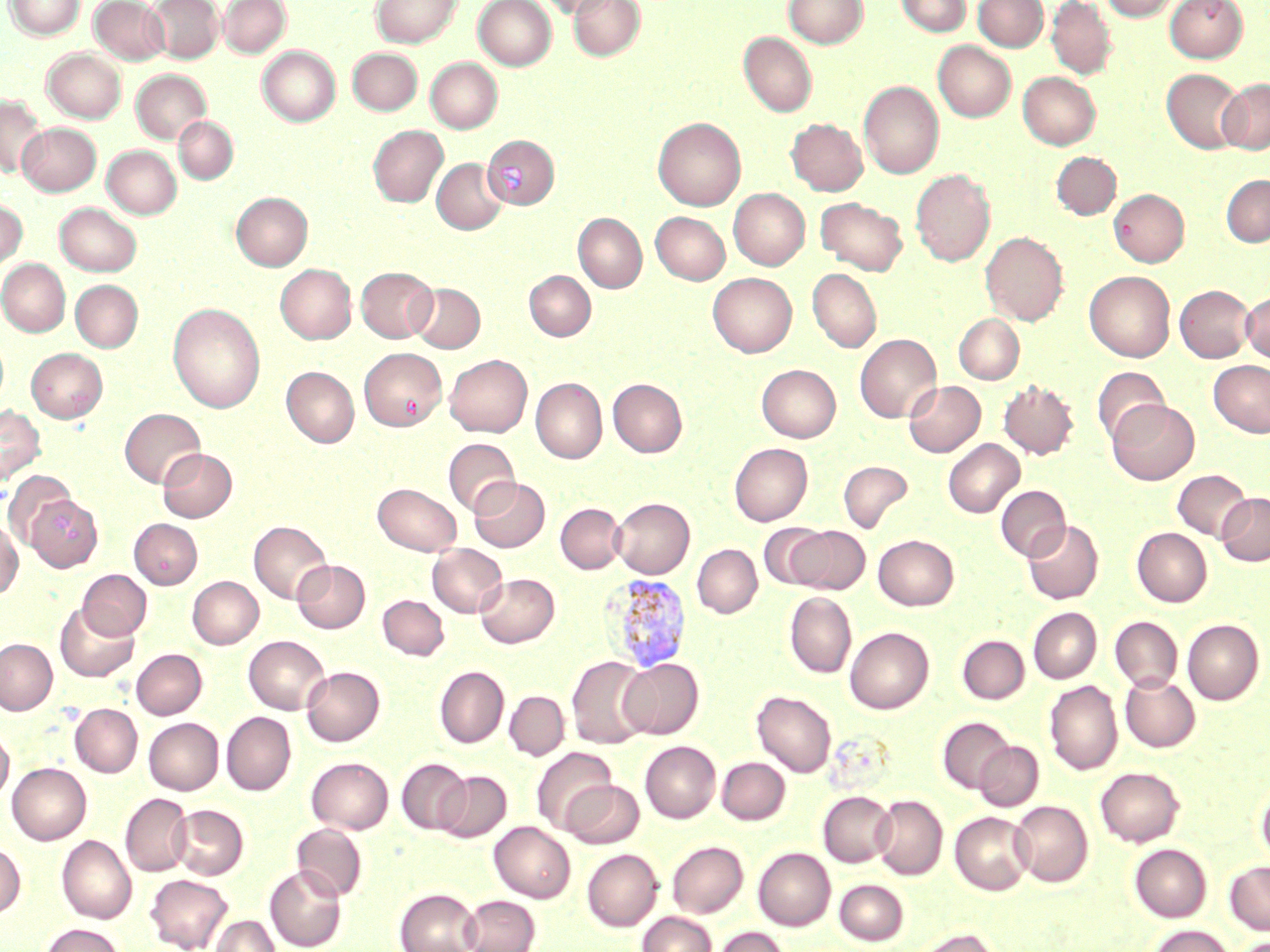

slide-level diagnosis = Plasmodium vivax
uninfected red blood cell locations = approximate bounding boxes as named x1/y1/x2/y2 corners in pixels: (x1=4, y1=0, x2=85, y2=40), (x1=90, y1=0, x2=169, y2=65), (x1=146, y1=0, x2=223, y2=63), (x1=219, y1=0, x2=291, y2=57), (x1=371, y1=0, x2=462, y2=47), (x1=474, y1=0, x2=556, y2=70), (x1=539, y1=0, x2=616, y2=18), (x1=569, y1=0, x2=644, y2=61), (x1=784, y1=0, x2=867, y2=49), (x1=896, y1=0, x2=971, y2=36), (x1=973, y1=0, x2=1048, y2=51), (x1=1046, y1=0, x2=1116, y2=79), (x1=1099, y1=0, x2=1182, y2=21), (x1=1165, y1=0, x2=1248, y2=62), (x1=739, y1=32, x2=817, y2=116), (x1=933, y1=41, x2=1016, y2=121), (x1=258, y1=46, x2=340, y2=126), (x1=348, y1=48, x2=421, y2=115), (x1=43, y1=49, x2=126, y2=122), (x1=426, y1=58, x2=502, y2=133), (x1=1162, y1=68, x2=1246, y2=153), (x1=131, y1=70, x2=210, y2=144), (x1=1018, y1=71, x2=1100, y2=149), (x1=1219, y1=78, x2=1270, y2=154), (x1=859, y1=80, x2=943, y2=179), (x1=0, y1=96, x2=46, y2=179), (x1=174, y1=116, x2=238, y2=184), (x1=653, y1=117, x2=745, y2=210), (x1=786, y1=118, x2=868, y2=195), (x1=17, y1=122, x2=101, y2=196), (x1=368, y1=126, x2=448, y2=207), (x1=483, y1=135, x2=559, y2=209), (x1=102, y1=145, x2=181, y2=218), (x1=1052, y1=152, x2=1121, y2=219), (x1=432, y1=158, x2=507, y2=234), (x1=910, y1=168, x2=995, y2=267), (x1=1221, y1=175, x2=1270, y2=246), (x1=1109, y1=188, x2=1189, y2=266), (x1=729, y1=189, x2=809, y2=269), (x1=231, y1=192, x2=312, y2=270), (x1=815, y1=197, x2=908, y2=275), (x1=0, y1=198, x2=27, y2=270), (x1=55, y1=203, x2=141, y2=276), (x1=651, y1=212, x2=729, y2=284), (x1=573, y1=213, x2=646, y2=292), (x1=980, y1=231, x2=1068, y2=325), (x1=0, y1=259, x2=70, y2=336), (x1=276, y1=264, x2=356, y2=344), (x1=356, y1=267, x2=437, y2=342), (x1=807, y1=268, x2=882, y2=352), (x1=1085, y1=270, x2=1175, y2=362), (x1=525, y1=271, x2=595, y2=341), (x1=708, y1=273, x2=796, y2=357), (x1=70, y1=280, x2=142, y2=352), (x1=409, y1=283, x2=485, y2=352), (x1=1175, y1=285, x2=1254, y2=362), (x1=1241, y1=290, x2=1270, y2=363), (x1=167, y1=302, x2=265, y2=413), (x1=954, y1=314, x2=1024, y2=384), (x1=855, y1=334, x2=941, y2=422), (x1=359, y1=347, x2=446, y2=431), (x1=27, y1=348, x2=107, y2=422), (x1=444, y1=354, x2=532, y2=437), (x1=1209, y1=359, x2=1270, y2=437), (x1=757, y1=364, x2=841, y2=441), (x1=1092, y1=366, x2=1169, y2=446), (x1=281, y1=367, x2=359, y2=446), (x1=531, y1=378, x2=607, y2=463), (x1=608, y1=378, x2=687, y2=457), (x1=904, y1=380, x2=985, y2=457), (x1=998, y1=380, x2=1079, y2=460), (x1=1108, y1=399, x2=1200, y2=485), (x1=0, y1=405, x2=45, y2=485), (x1=120, y1=409, x2=205, y2=487), (x1=443, y1=438, x2=520, y2=516), (x1=943, y1=439, x2=1024, y2=517), (x1=730, y1=443, x2=812, y2=525), (x1=158, y1=448, x2=236, y2=521), (x1=838, y1=461, x2=913, y2=533), (x1=1173, y1=469, x2=1252, y2=541), (x1=4, y1=470, x2=76, y2=547), (x1=469, y1=477, x2=549, y2=552), (x1=373, y1=484, x2=461, y2=555), (x1=996, y1=485, x2=1070, y2=561), (x1=17, y1=489, x2=101, y2=568), (x1=1217, y1=492, x2=1270, y2=565), (x1=612, y1=497, x2=694, y2=578), (x1=555, y1=503, x2=627, y2=574), (x1=130, y1=519, x2=202, y2=588), (x1=1022, y1=519, x2=1103, y2=604), (x1=0, y1=520, x2=22, y2=599), (x1=249, y1=521, x2=332, y2=604), (x1=758, y1=522, x2=832, y2=590), (x1=790, y1=526, x2=870, y2=594), (x1=1132, y1=527, x2=1212, y2=606), (x1=873, y1=535, x2=959, y2=610), (x1=428, y1=544, x2=507, y2=617), (x1=692, y1=544, x2=762, y2=618), (x1=292, y1=559, x2=370, y2=633), (x1=78, y1=569, x2=151, y2=640), (x1=475, y1=573, x2=559, y2=647), (x1=188, y1=576, x2=263, y2=649), (x1=785, y1=592, x2=856, y2=678), (x1=378, y1=595, x2=449, y2=660), (x1=55, y1=602, x2=139, y2=682), (x1=1028, y1=608, x2=1101, y2=683), (x1=1110, y1=617, x2=1183, y2=691), (x1=1183, y1=619, x2=1264, y2=704), (x1=845, y1=627, x2=933, y2=713), (x1=958, y1=635, x2=1029, y2=703), (x1=244, y1=636, x2=330, y2=714), (x1=0, y1=639, x2=57, y2=714), (x1=132, y1=649, x2=206, y2=719), (x1=567, y1=656, x2=653, y2=748), (x1=619, y1=658, x2=703, y2=739), (x1=301, y1=666, x2=384, y2=746), (x1=434, y1=666, x2=509, y2=747), (x1=1120, y1=674, x2=1200, y2=752), (x1=1044, y1=680, x2=1123, y2=774), (x1=505, y1=691, x2=569, y2=759), (x1=752, y1=691, x2=836, y2=777), (x1=70, y1=703, x2=142, y2=777), (x1=222, y1=712, x2=296, y2=794), (x1=144, y1=717, x2=223, y2=794), (x1=938, y1=717, x2=1015, y2=793), (x1=0, y1=727, x2=14, y2=803), (x1=640, y1=741, x2=720, y2=822), (x1=975, y1=742, x2=1043, y2=810), (x1=532, y1=747, x2=617, y2=834), (x1=307, y1=757, x2=393, y2=833), (x1=717, y1=757, x2=790, y2=824), (x1=397, y1=758, x2=471, y2=833), (x1=7, y1=763, x2=91, y2=844), (x1=1096, y1=766, x2=1184, y2=846), (x1=436, y1=771, x2=511, y2=842), (x1=562, y1=780, x2=644, y2=848), (x1=1256, y1=780, x2=1270, y2=866), (x1=818, y1=791, x2=896, y2=867), (x1=121, y1=793, x2=192, y2=876), (x1=872, y1=795, x2=947, y2=880), (x1=1010, y1=800, x2=1093, y2=886), (x1=170, y1=804, x2=248, y2=879), (x1=950, y1=811, x2=1034, y2=894), (x1=489, y1=822, x2=575, y2=902), (x1=292, y1=823, x2=367, y2=901), (x1=57, y1=835, x2=136, y2=923), (x1=668, y1=841, x2=748, y2=917), (x1=0, y1=843, x2=25, y2=918), (x1=1130, y1=844, x2=1211, y2=921), (x1=753, y1=848, x2=835, y2=930), (x1=582, y1=849, x2=662, y2=930), (x1=1225, y1=861, x2=1270, y2=935), (x1=265, y1=865, x2=346, y2=950), (x1=145, y1=874, x2=233, y2=952), (x1=834, y1=879, x2=908, y2=945), (x1=395, y1=888, x2=482, y2=952), (x1=460, y1=895, x2=540, y2=952), (x1=638, y1=912, x2=717, y2=952), (x1=210, y1=915, x2=280, y2=952), (x1=41, y1=923, x2=125, y2=952), (x1=1149, y1=925, x2=1233, y2=952), (x1=715, y1=927, x2=791, y2=952), (x1=912, y1=928, x2=1001, y2=952)
field of view = single
modality = optical microscopy
magnification = 1000x
Plasmodium vivax-infected red blood cell locations = approximate bounding boxes as named x1/y1/x2/y2 corners in pixels: (x1=603, y1=573, x2=692, y2=673)
image size = 1270×952 pixels
preparation = thin blood film
stain = May-Grünwald-Giemsa